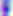
Summary:
  - Modality: photomicrograph
  - Magnification: 400x
  - Identification: Toxoplasma gondii